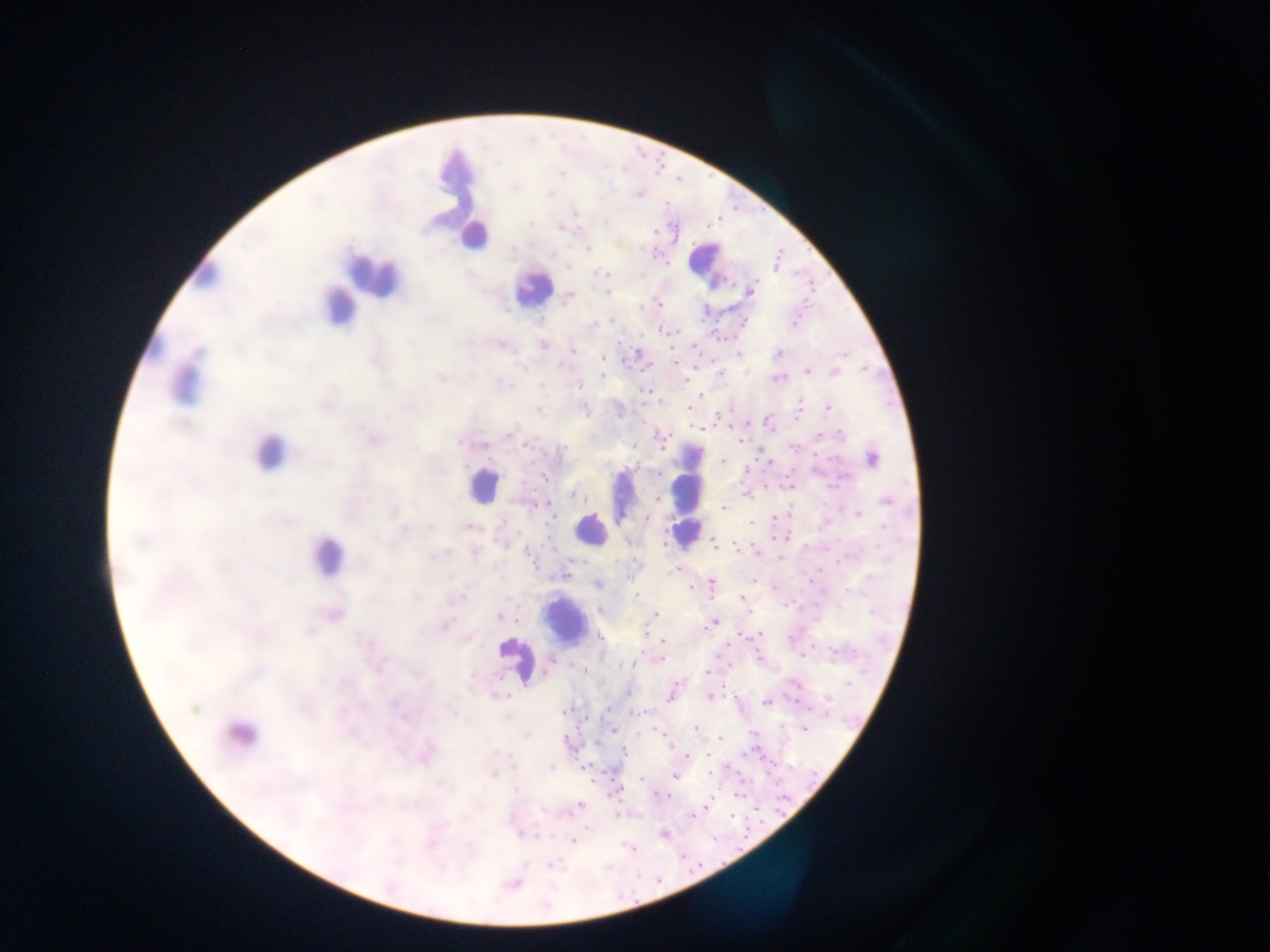
Approximate centers as x y in pixels.
Summary:
  - Leukocyte locations: 456 175; 474 234; 705 262; 203 273; 372 273; 532 288; 340 307; 185 380; 269 452; 483 485; 687 485; 688 525; 590 529; 686 532; 326 555; 565 623; 515 660; 239 735
  - Plasmodium parasite locations: 736 207; 720 219; 709 226; 656 231; 589 250; 780 250; 655 254; 668 263; 775 265; 596 269; 798 274; 811 281; 812 289; 750 290; 608 292; 569 296; 805 302; 659 303; 641 305; 800 314; 721 316; 539 319; 702 319; 613 320; 743 321; 796 323; 713 330; 660 331; 680 332; 643 334; 666 335; 725 337; 735 337; 719 338; 694 342; 543 344; 619 344; 573 350; 673 350; 638 353; 701 353; 739 353; 779 353; 847 355; 602 358; 623 360; 711 360; 677 362; 695 367; 864 367; 631 369; 641 369; 807 369; 834 371; 721 373; 603 375; 441 376; 779 377; 688 380; 578 385; 644 390; 700 394; 662 401; 801 402; 541 406; 827 407; 688 409; 800 409; 585 410; 632 411; 721 415; 766 416; 796 418; 747 423; 764 423; 644 424; 690 426; 730 427; 701 428; 774 431; 658 435; 820 435; 509 436; 670 436; 373 438; 742 441; 524 442; 799 445; 633 446; 791 446; 663 448; 816 453; 758 458; 870 458; 532 459; 828 459; 723 461; 639 463; 770 463; 748 469; 791 469; 544 474; 658 474; 535 486; 766 486; 789 486; 575 493; 745 494; 657 497; 887 500; 550 502; 537 504; 723 508; 858 514; 645 519; 775 519; 750 522; 548 525; 470 526; 784 537; 542 542; 630 542; 714 542; 753 543; 807 544; 736 548; 828 549; 846 553; 758 554; 780 558; 836 560; 573 561; 585 562; 538 566; 678 568; 822 571; 565 575; 629 578; 756 580; 809 581; 711 583; 598 584; 775 585; 690 587; 846 589; 638 596; 742 598; 796 599; 787 606; 599 609; 751 610; 871 610; 333 613; 502 614; 654 615; 518 621; 713 623; 444 624; 740 632; 646 633; 757 635; 602 637; 663 640; 728 644; 756 647; 835 652; 854 652; 643 653; 803 654; 719 655; 760 658; 550 660; 657 660; 634 664; 729 665; 865 670; 583 671; 709 671; 678 682; 848 682; 796 684; 724 687; 628 692; 671 695; 710 696; 736 697; 828 697; 767 702; 394 703; 798 703; 610 707; 566 709; 645 712; 632 714; 601 716; 587 718; 578 725; 696 726; 805 728; 614 731; 660 731; 753 733; 664 736; 567 737; 720 739; 597 742; 671 746; 756 750; 744 752; 623 753; 709 753; 424 755; 686 756; 763 757; 682 759; 776 760; 585 765; 727 766; 549 767; 791 767; 604 771; 709 772; 740 772; 769 772; 494 773; 815 774; 674 776; 641 779; 593 780; 776 785; 618 790; 655 794; 736 794; 714 795; 743 795; 668 796; 786 797; 579 805; 704 807; 776 808; 757 809; 784 811; 693 814; 733 814; 748 818; 511 822; 762 822; 749 827; 536 833; 664 834; 522 836; 714 836; 746 837; 573 840; 741 848; 632 849; 684 856; 563 860; 701 865; 549 866; 691 872; 512 883
  - Field of view: single
  - Capture: mobile-phone photograph through a microscope
  - Country: Ghana
  - Preparation: thick blood smear
  - Image size: 1270×952 pixels